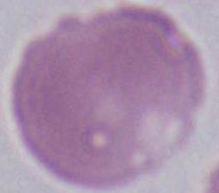 Micrograph. A red blood cell is shown. Captured at 1000x magnification.